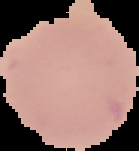
malaria_status: uninfected
preparation: thin blood film
image_type: cell region segmented out of the field of view; surrounding area masked to black
image_size: 139×151 pixels